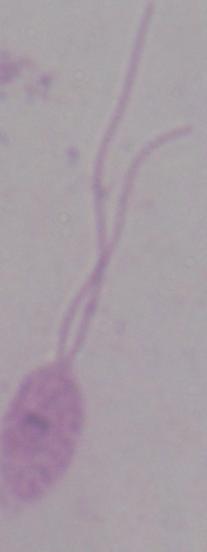

modality = micrograph
identification = Leishmania
magnification = 1000x